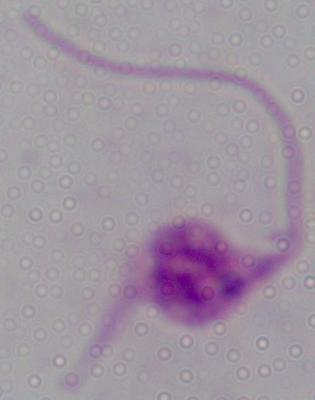
A Leishmania parasite is seen. 1000x magnification. Photomicrograph.